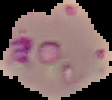

preparation = thin blood smear
malaria status = parasitized
image type = segmented cell region on a black background
image size = 112×100 pixels